Report the malaria status of this cell.
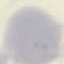
It is uninfected.

Summary:
  - Preparation: thin smear
  - Capture: smartphone camera at the microscope eyepiece
  - Stain: Giemsa
  - Image type: cell patch, automatically extracted from a larger field of view and resized to 64 × 64 pixels